Locate and identify every blood parasite.
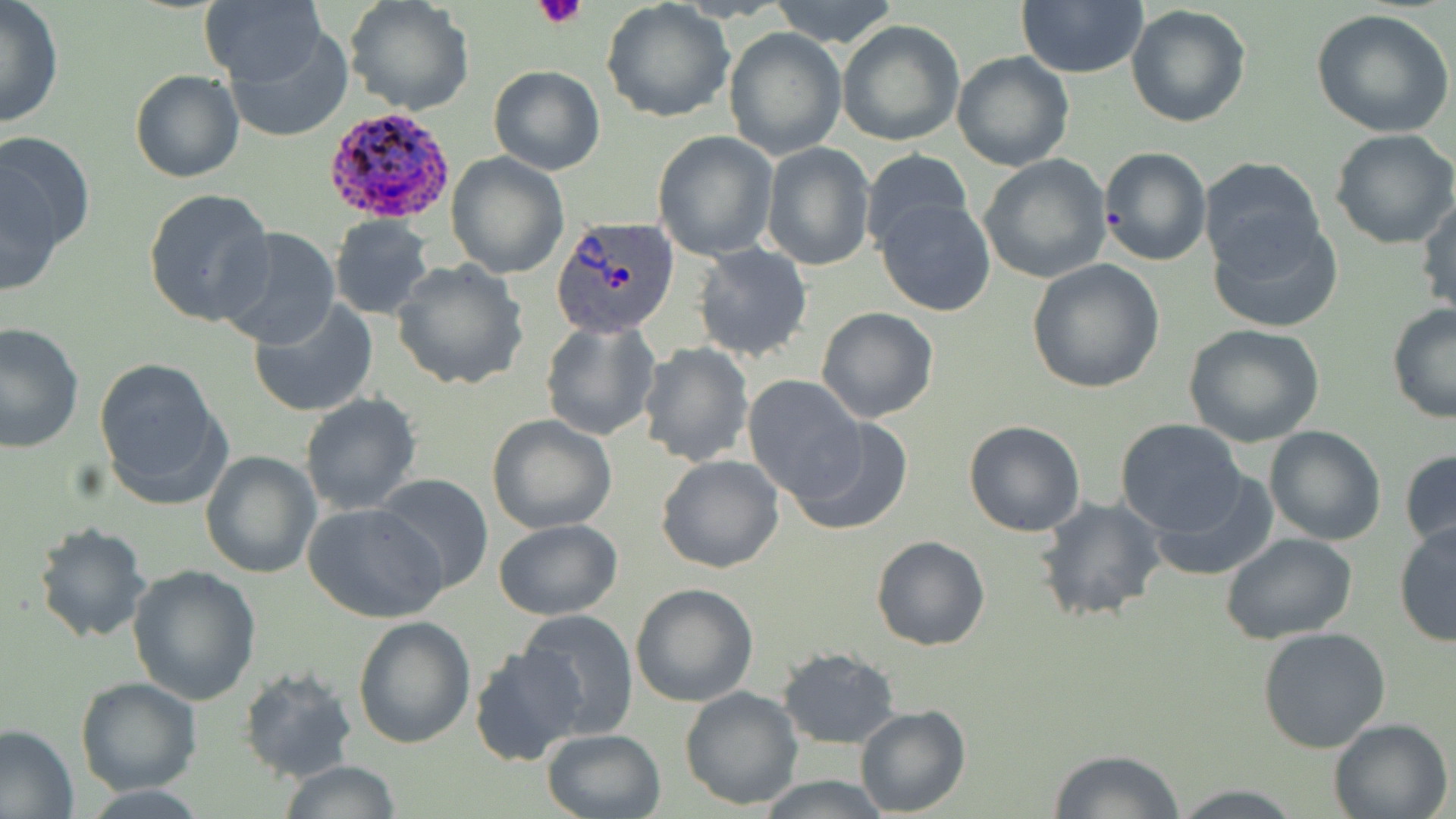

Approximate bounding boxes as (x1, y1, x2, y2) in pixels.
Plasmodium ovale-infected red blood cells: (321, 107, 452, 223), (553, 216, 679, 339).
No Plasmodium falciparum, Plasmodium malariae, Plasmodium vivax, Babesia divergens, or Trypanosoma brucei observed.

Uninfected red blood cell locations: (201, 0, 326, 88), (345, 0, 475, 116), (768, 0, 901, 47), (1014, 0, 1148, 80), (0, 2, 63, 129), (602, 2, 734, 122), (1125, 5, 1253, 129), (1312, 9, 1456, 139), (836, 19, 966, 148), (224, 24, 353, 143), (723, 26, 847, 159), (951, 50, 1075, 171), (488, 64, 605, 176), (130, 69, 243, 183), (1329, 128, 1456, 249), (0, 129, 94, 267), (651, 131, 780, 261), (760, 143, 875, 272), (1098, 146, 1210, 267), (861, 149, 974, 256), (445, 151, 568, 278), (978, 155, 1113, 284), (1199, 156, 1327, 271), (0, 168, 64, 297), (144, 188, 273, 327), (1416, 193, 1456, 321), (875, 198, 998, 318), (329, 215, 435, 319), (1207, 215, 1344, 334), (214, 227, 342, 351), (693, 243, 812, 362), (659, 247, 794, 430), (1025, 258, 1167, 394), (392, 261, 531, 391), (247, 298, 380, 418), (1386, 302, 1456, 423), (815, 307, 940, 425), (541, 321, 661, 441), (0, 322, 83, 452), (1182, 323, 1326, 447), (639, 342, 754, 467), (94, 359, 226, 506), (742, 374, 868, 503), (299, 393, 422, 515), (487, 414, 617, 533), (789, 416, 915, 535), (1114, 418, 1249, 537), (963, 419, 1086, 536), (1262, 425, 1388, 547), (1399, 448, 1455, 557), (200, 451, 322, 577), (656, 454, 784, 573), (1147, 469, 1279, 583), (372, 474, 495, 597), (1035, 496, 1168, 626), (304, 502, 449, 623), (492, 520, 623, 618), (32, 521, 153, 644), (1392, 521, 1456, 648), (1221, 532, 1357, 644), (871, 535, 990, 651), (127, 564, 260, 704), (630, 582, 759, 707), (514, 610, 640, 739), (352, 615, 475, 750), (1257, 626, 1391, 753), (470, 643, 586, 767), (778, 647, 901, 749), (240, 664, 357, 782), (75, 677, 201, 794), (678, 685, 804, 810), (855, 705, 970, 816), (1329, 717, 1456, 819), (0, 721, 79, 819), (540, 728, 666, 818), (1048, 748, 1184, 819), (279, 759, 402, 818), (754, 775, 893, 818), (1170, 783, 1305, 818). Platelet locations: (533, 3, 587, 31). Slide-level diagnosis: Plasmodium ovale. Light microscopy. Thin blood film. Image is 1456×819 pixels. May-Grünwald-Giemsa stain. Captured at 1000x magnification. Single field of view.